Identify the preparation type.
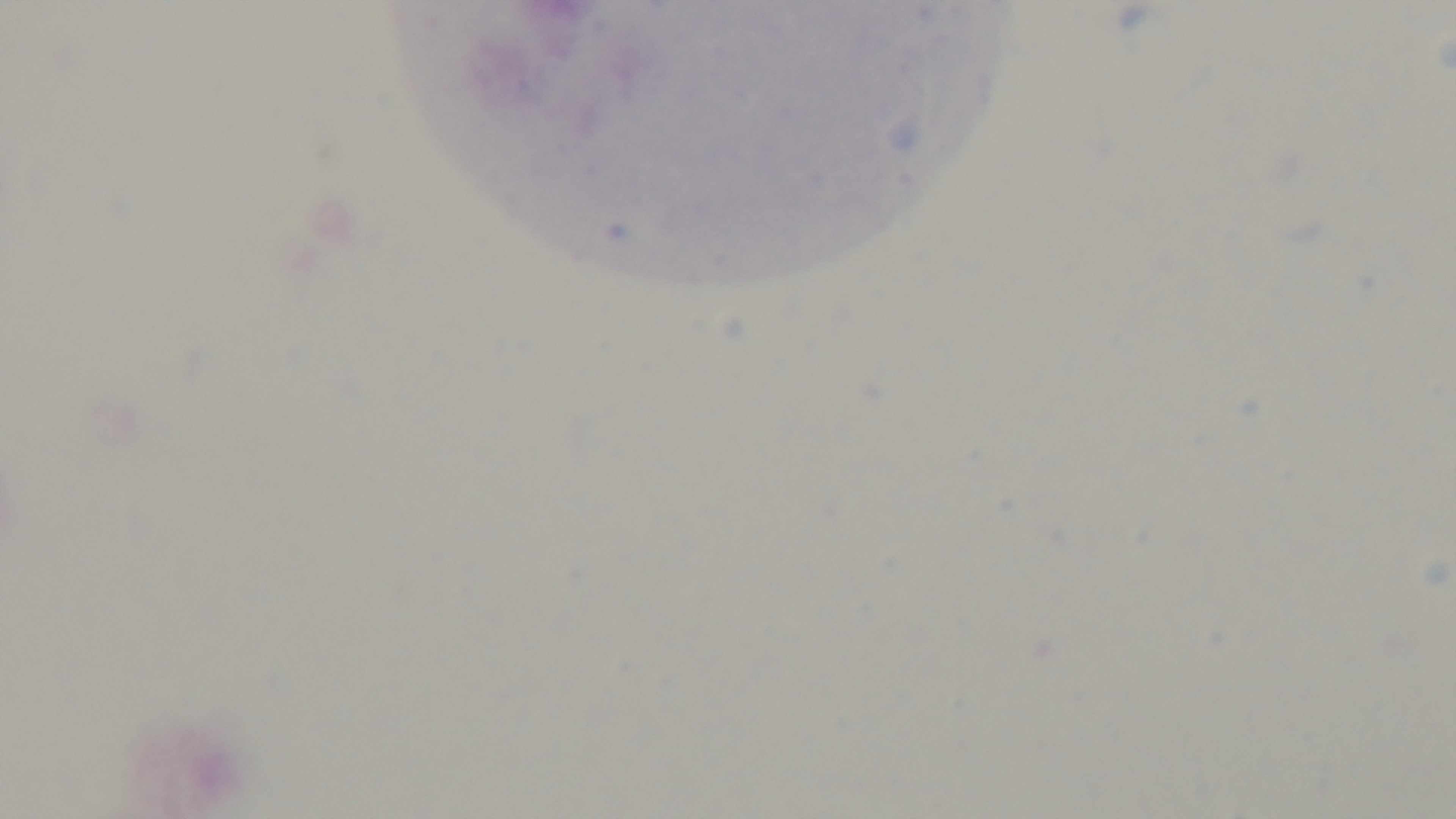

It is a thick blood film.

field of view = one from the slide
stain = Giemsa
capture = mounted 4K digital camera
modality = light microscopy
objective = 100x oil immersion
malaria status = negative